Report the malaria status of this cell.
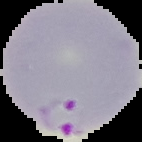

Parasitized.

The area outside the segmented cell region is set to black. From a thin blood smear. Image is 142×142 pixels.